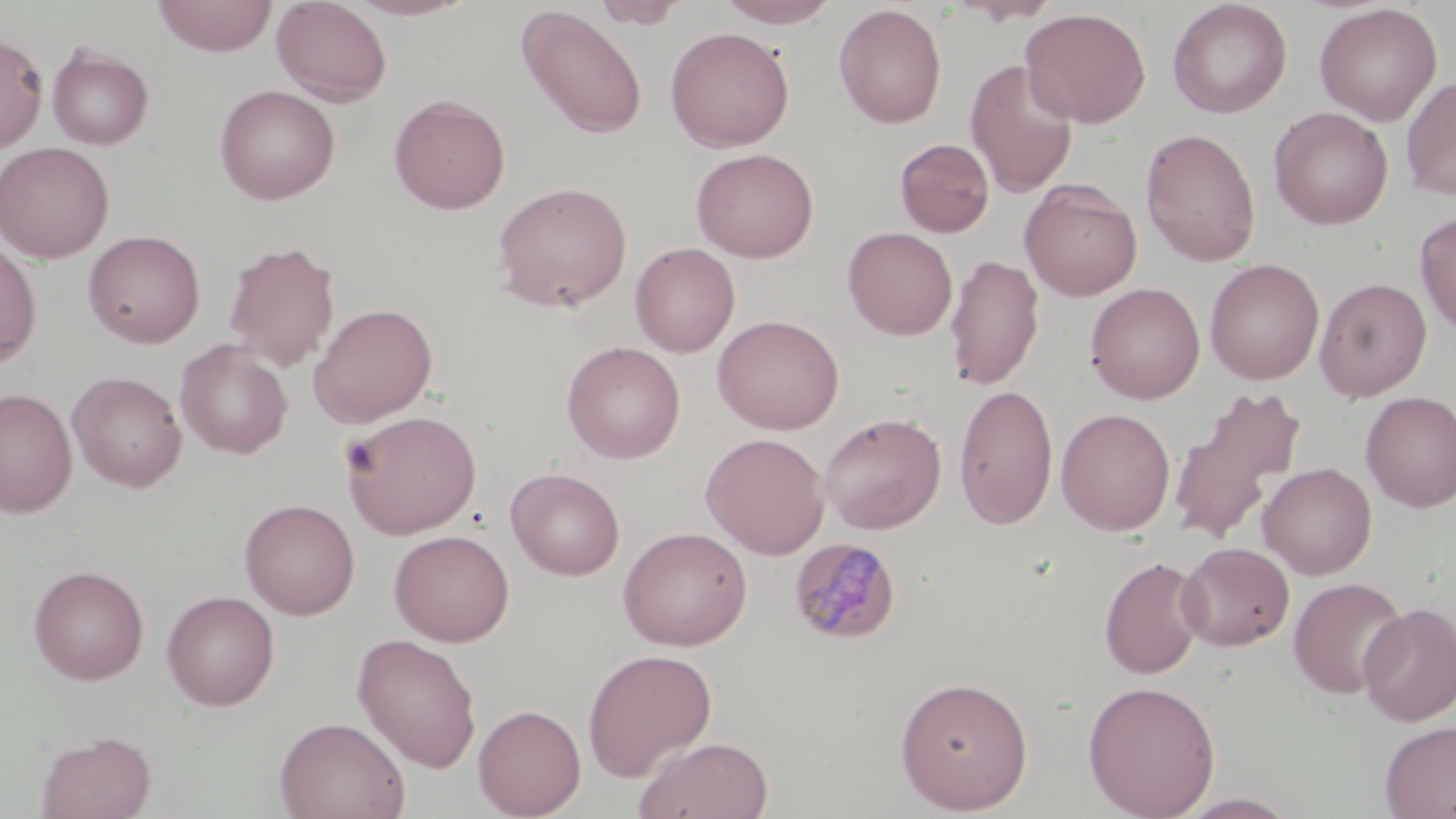
Approximate bounding boxes as (x1, y1, x2, y2) in pixels. Uninfected red blood cell locations: (153, 0, 278, 56), (271, 0, 393, 106), (345, 0, 474, 20), (593, 0, 689, 29), (715, 0, 843, 27), (953, 0, 1061, 25), (1168, 1, 1292, 118), (833, 4, 947, 129), (1314, 4, 1442, 125), (517, 5, 648, 139), (1019, 7, 1151, 128), (665, 26, 795, 152), (0, 33, 48, 152), (47, 45, 154, 150), (964, 59, 1079, 198), (1401, 76, 1456, 200), (213, 84, 340, 205), (389, 93, 510, 214), (1268, 106, 1393, 229), (1140, 128, 1261, 266), (894, 138, 995, 237), (0, 141, 115, 263), (691, 147, 819, 262), (1020, 180, 1142, 301), (492, 181, 632, 312), (1415, 211, 1456, 336), (843, 227, 957, 340), (83, 229, 206, 348), (0, 239, 42, 367), (223, 239, 341, 371), (630, 242, 740, 357), (944, 253, 1043, 391), (1204, 258, 1325, 384), (1314, 277, 1432, 401), (1084, 282, 1205, 404), (308, 302, 438, 427), (712, 314, 845, 434), (175, 339, 293, 459), (562, 341, 686, 464), (67, 370, 187, 492), (954, 383, 1059, 529), (0, 387, 77, 517), (1167, 387, 1309, 548), (1360, 391, 1456, 511), (1056, 407, 1175, 535), (341, 409, 482, 538), (819, 412, 946, 534), (701, 432, 830, 559), (1258, 462, 1377, 579), (506, 467, 625, 580), (239, 498, 361, 619), (617, 526, 753, 650), (389, 529, 515, 646), (1176, 542, 1294, 651), (1098, 555, 1208, 678), (28, 564, 150, 685), (1287, 576, 1410, 699), (161, 589, 280, 710), (1357, 602, 1456, 726), (352, 633, 482, 773), (582, 648, 717, 782), (894, 675, 1034, 813), (1082, 679, 1221, 818), (473, 704, 586, 819), (274, 716, 410, 819), (1379, 720, 1456, 819), (35, 729, 157, 819), (633, 736, 774, 819), (1174, 792, 1301, 818). Platelet locations: (341, 438, 381, 478). Plasmodium malariae-infected red blood cell locations: (788, 536, 903, 645). Slide-level diagnosis: Plasmodium malariae. Single field of view. Thin blood film. 1000x magnification. Image is 1456×819 pixels. May-Grünwald-Giemsa stain. Light microscopy.